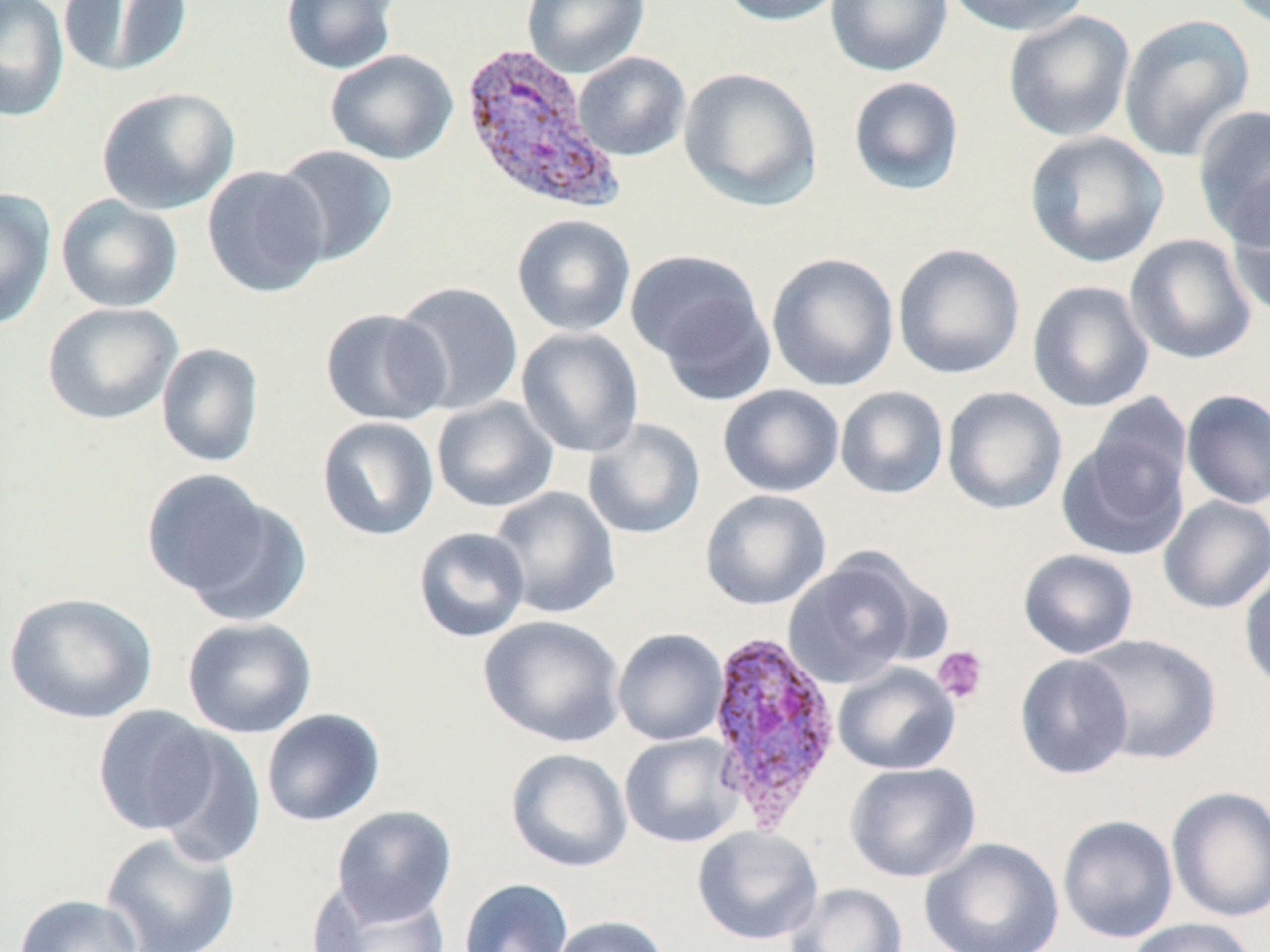 Approximate bounding boxes as (x1,y1)-(x2,y2) corner pairs in pixels. Plasmodium vivax-infected red blood cell locations: (459,42)-(623,216), (704,627)-(843,829). Uninfected red blood cell locations: (0,0)-(69,121), (58,0)-(192,78), (280,0)-(400,75), (522,0)-(650,78), (717,0)-(848,26), (825,0)-(952,77), (941,0)-(1092,37), (1003,10)-(1136,143), (1118,13)-(1255,162), (324,49)-(458,165), (573,52)-(691,162), (678,67)-(823,210), (848,76)-(965,196), (96,86)-(239,215), (1191,104)-(1270,246), (1023,130)-(1170,269), (272,144)-(399,266), (202,165)-(331,298), (1223,179)-(1270,319), (0,187)-(57,331), (56,194)-(183,313), (511,214)-(637,336), (1124,233)-(1257,365), (892,243)-(1025,379), (625,249)-(765,367), (766,252)-(899,392), (1027,280)-(1155,413), (391,281)-(524,415), (653,289)-(777,407), (41,301)-(183,425), (319,307)-(452,426), (516,327)-(644,458), (156,342)-(265,468), (718,384)-(845,498), (835,386)-(949,499), (942,386)-(1067,515), (1181,389)-(1270,510), (1087,393)-(1193,505), (431,396)-(559,513), (316,417)-(440,541), (583,418)-(706,539), (1057,435)-(1189,562), (141,471)-(296,613), (488,486)-(621,619), (700,489)-(831,610), (1158,495)-(1270,614), (413,526)-(531,643), (1018,548)-(1140,659), (783,552)-(923,689), (1239,567)-(1270,694), (3,592)-(158,725), (478,615)-(626,747), (182,617)-(317,738), (612,628)-(728,745), (1077,634)-(1222,765), (1014,654)-(1134,779), (833,662)-(960,775), (92,705)-(220,836), (261,708)-(386,827), (148,726)-(268,869), (619,733)-(744,848), (504,748)-(632,873), (844,761)-(981,883), (1166,785)-(1270,923), (331,805)-(458,925), (1057,814)-(1179,944), (692,826)-(823,946), (101,831)-(241,952), (919,837)-(1065,952), (458,878)-(573,952), (308,882)-(453,952), (785,883)-(907,952), (14,894)-(145,952), (549,915)-(671,952), (1126,917)-(1258,952). Platelet locations: (932,645)-(989,704). Slide-level diagnosis: Plasmodium vivax. Thin blood film. Image is 1270×952 pixels. May-Grünwald-Giemsa-stained preparation. One field of a larger specimen. Light microscopy. Captured at 1000x magnification.